Assess this cell for malaria.
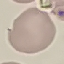

Uninfected.

Summary:
  - Capture: smartphone through the microscope eyepiece
  - Preparation: thin blood smear
  - Image type: cell patch, automatically extracted from a larger field of view and resized to 64 × 64 pixels
  - Stain: Giemsa